Point out each malaria parasite.
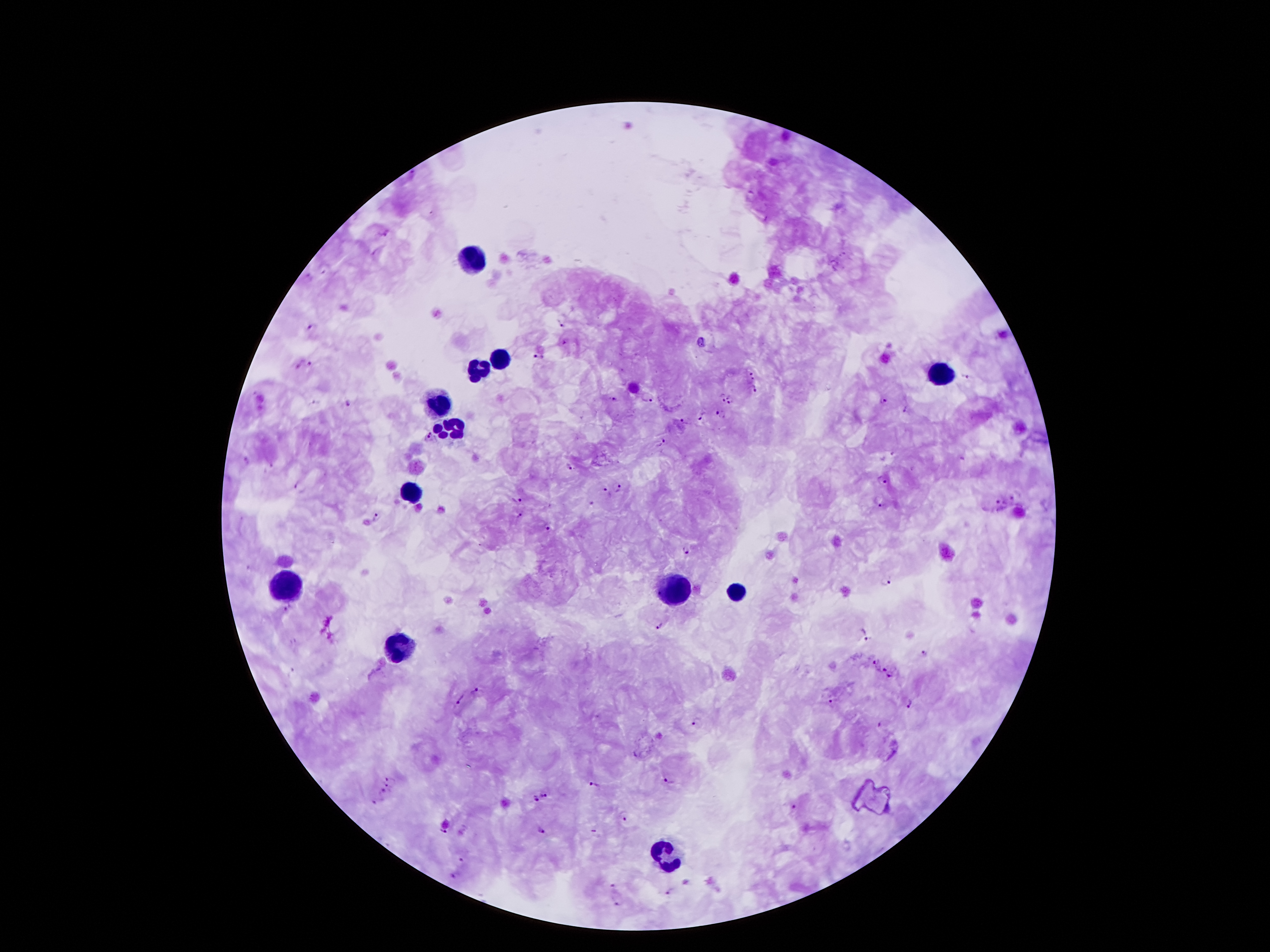
Approximate centers as {x, y} in pixels.
Malaria parasites: {386, 234}, {560, 323}, {312, 328}, {566, 341}, {702, 343}, {539, 357}, {310, 364}, {297, 365}, {750, 371}, {966, 376}, {752, 380}, {754, 390}, {613, 398}, {649, 398}, {721, 398}, {732, 399}, {883, 401}, {350, 403}, {904, 409}, {720, 413}, {700, 416}, {685, 422}, {429, 435}, {662, 442}, {247, 461}, {572, 467}, {882, 477}, {299, 487}, {620, 488}, {604, 489}, {1013, 497}, {517, 499}, {998, 500}, {881, 503}, {590, 504}, {519, 514}, {376, 518}, {547, 527}, {686, 550}, {888, 580}, {288, 607}, {661, 624}, {867, 639}, {922, 651}, {873, 661}, {882, 668}, {892, 677}, {476, 690}, {462, 700}, {832, 701}, {910, 703}, {696, 721}, {878, 723}, {637, 754}, {390, 777}, {669, 779}, {592, 782}, {387, 786}, {382, 792}, {546, 794}, {535, 800}, {376, 803}, {794, 807}, {625, 817}, {542, 829}, {445, 831}, {593, 831}, {460, 858}, {456, 876}, {613, 886}, {669, 892}, {617, 904}.

Summary:
  - Leukocyte locations: {473, 260}, {503, 357}, {480, 370}, {939, 370}, {442, 400}, {450, 426}, {411, 490}, {285, 582}, {674, 594}, {737, 594}, {401, 650}, {669, 853}
  - Patient malaria status: positive for Plasmodium falciparum
  - Preparation: thick peripheral-blood smear
  - Image size: 1270×952 pixels
  - Magnification: 100x
  - Field of view: single
  - Stain: Giemsa
  - Capture: smartphone through the microscope eyepiece